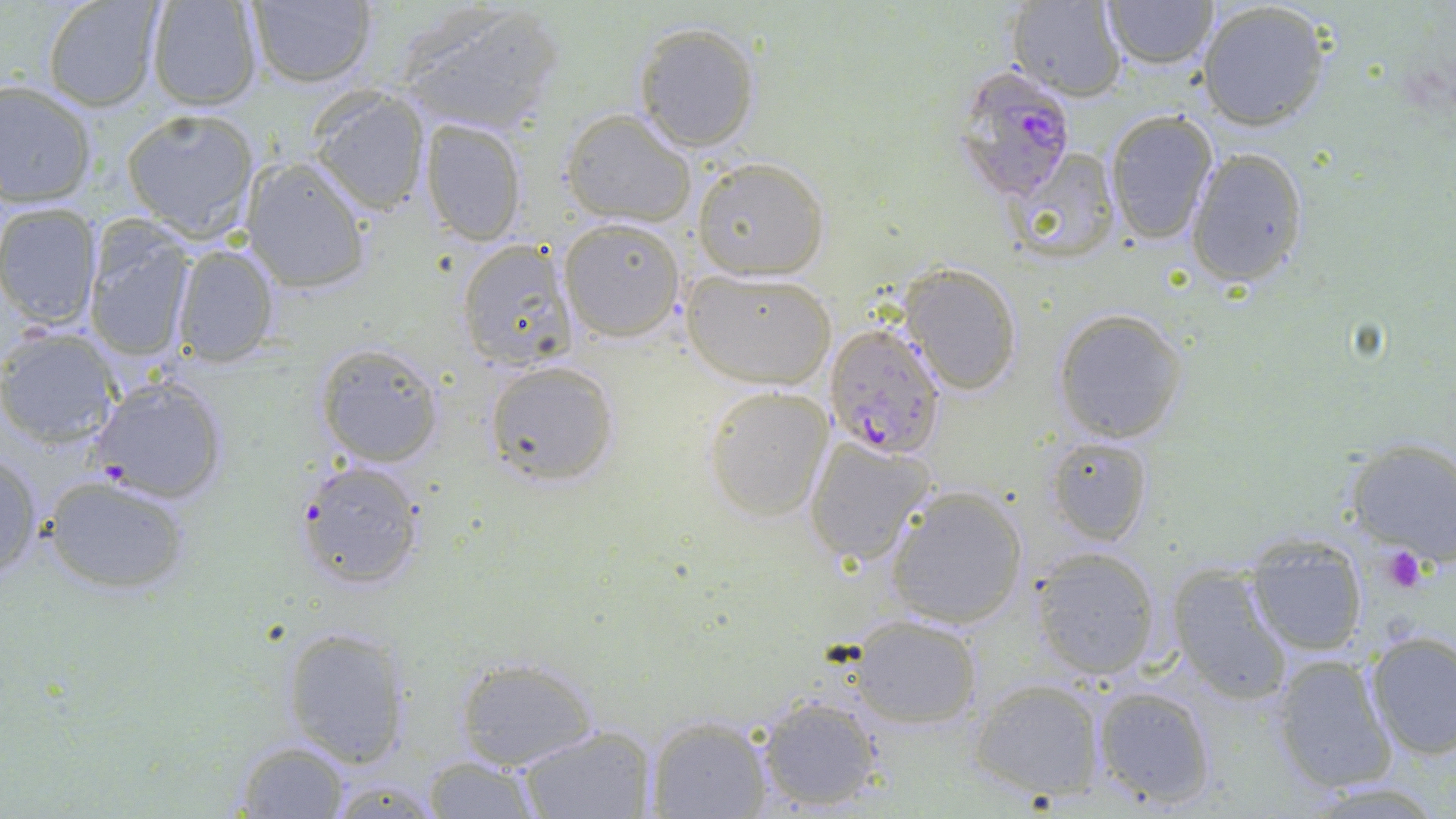

Summary:
  - Coordinate format: approximate bounding boxes as named x1/y1/x2/y2 corners in pixels
  - Uninfected red blood cell locations: (x1=392, y1=0, x2=566, y2=137), (x1=1101, y1=0, x2=1219, y2=73), (x1=144, y1=1, x2=263, y2=111), (x1=243, y1=1, x2=379, y2=88), (x1=1007, y1=1, x2=1128, y2=98), (x1=1198, y1=1, x2=1333, y2=130), (x1=42, y1=2, x2=164, y2=110), (x1=633, y1=21, x2=761, y2=152), (x1=0, y1=80, x2=98, y2=207), (x1=305, y1=85, x2=431, y2=217), (x1=123, y1=108, x2=258, y2=240), (x1=560, y1=108, x2=696, y2=227), (x1=1102, y1=108, x2=1221, y2=244), (x1=419, y1=117, x2=528, y2=248), (x1=1184, y1=147, x2=1309, y2=287), (x1=1001, y1=149, x2=1120, y2=267), (x1=240, y1=154, x2=373, y2=293), (x1=692, y1=157, x2=828, y2=279), (x1=0, y1=203, x2=103, y2=328), (x1=560, y1=217, x2=687, y2=343), (x1=83, y1=221, x2=196, y2=364), (x1=456, y1=239, x2=578, y2=372), (x1=170, y1=242, x2=280, y2=367), (x1=900, y1=262, x2=1023, y2=394), (x1=683, y1=269, x2=837, y2=389), (x1=1052, y1=307, x2=1188, y2=444), (x1=0, y1=325, x2=123, y2=450), (x1=315, y1=344, x2=445, y2=466), (x1=484, y1=359, x2=620, y2=486), (x1=87, y1=373, x2=231, y2=503), (x1=701, y1=384, x2=834, y2=522), (x1=1047, y1=435, x2=1153, y2=545), (x1=802, y1=437, x2=938, y2=569), (x1=1342, y1=440, x2=1456, y2=565), (x1=0, y1=449, x2=43, y2=587), (x1=293, y1=460, x2=424, y2=590), (x1=41, y1=473, x2=195, y2=594), (x1=887, y1=486, x2=1029, y2=629), (x1=1245, y1=531, x2=1371, y2=655), (x1=1032, y1=548, x2=1161, y2=680), (x1=1167, y1=562, x2=1293, y2=701), (x1=848, y1=614, x2=982, y2=728), (x1=279, y1=625, x2=411, y2=769), (x1=1364, y1=630, x2=1456, y2=760), (x1=1269, y1=653, x2=1398, y2=795), (x1=455, y1=656, x2=601, y2=770), (x1=969, y1=677, x2=1106, y2=802), (x1=1091, y1=684, x2=1216, y2=809), (x1=754, y1=694, x2=885, y2=814), (x1=645, y1=715, x2=774, y2=819), (x1=512, y1=723, x2=657, y2=819), (x1=232, y1=738, x2=354, y2=818), (x1=422, y1=756, x2=545, y2=816)
  - Platelet locations: (x1=1380, y1=547, x2=1431, y2=594)
  - Plasmodium falciparum-infected red blood cell locations: (x1=946, y1=65, x2=1078, y2=202), (x1=825, y1=325, x2=946, y2=458)
  - Slide-level diagnosis: Plasmodium falciparum
  - Field of view: single
  - Stain: May-Grünwald-Giemsa
  - Preparation: thin blood smear
  - Modality: optical microscopy
  - Image size: 1456×819 pixels
  - Magnification: 1000x